Report the malaria status of this cell.
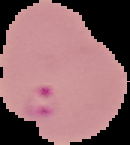
It is parasitized.

Image is 130×145 pixels. From a thin blood film. Cell region segmented out of the field of view; the surrounding area is masked to black.